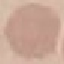
malaria_status: uninfected
stain: Giemsa
preparation: thin blood film
image_type: automatically extracted cell patch, resized to 64 × 64 pixels
capture: smartphone through the microscope eyepiece